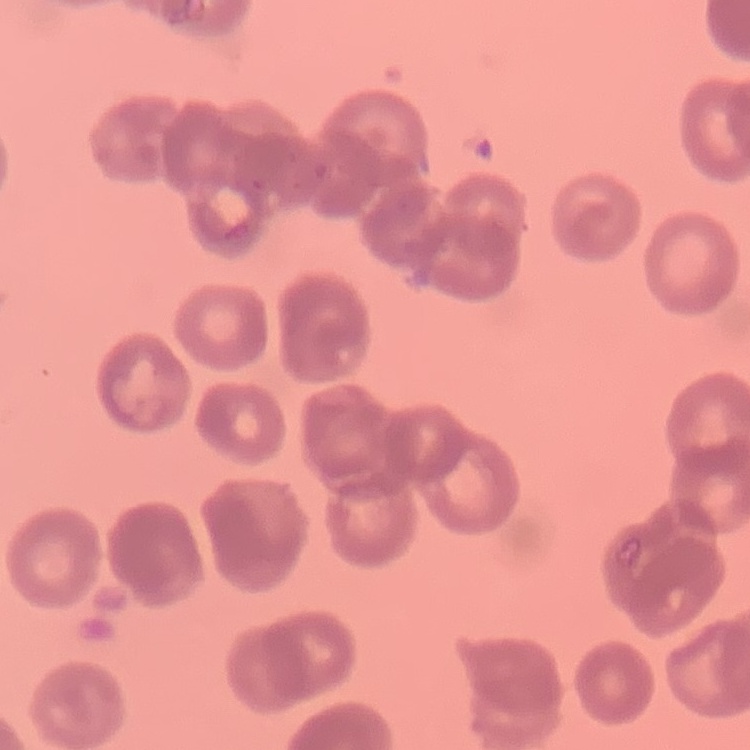
red_blood_cell_morphology: rouleaux formation
stain: Field's or Giemsa
image_type: square crop of a larger photomicrograph
preparation: thin blood film